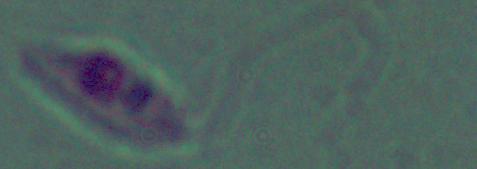

{
  "magnification": "1000x",
  "modality": "micrograph",
  "identification": "Leishmania"
}